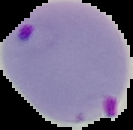

image size = 133×130 pixels
image type = segmented cell region on a black background
preparation = thin blood film
result = Plasmodium parasites detected